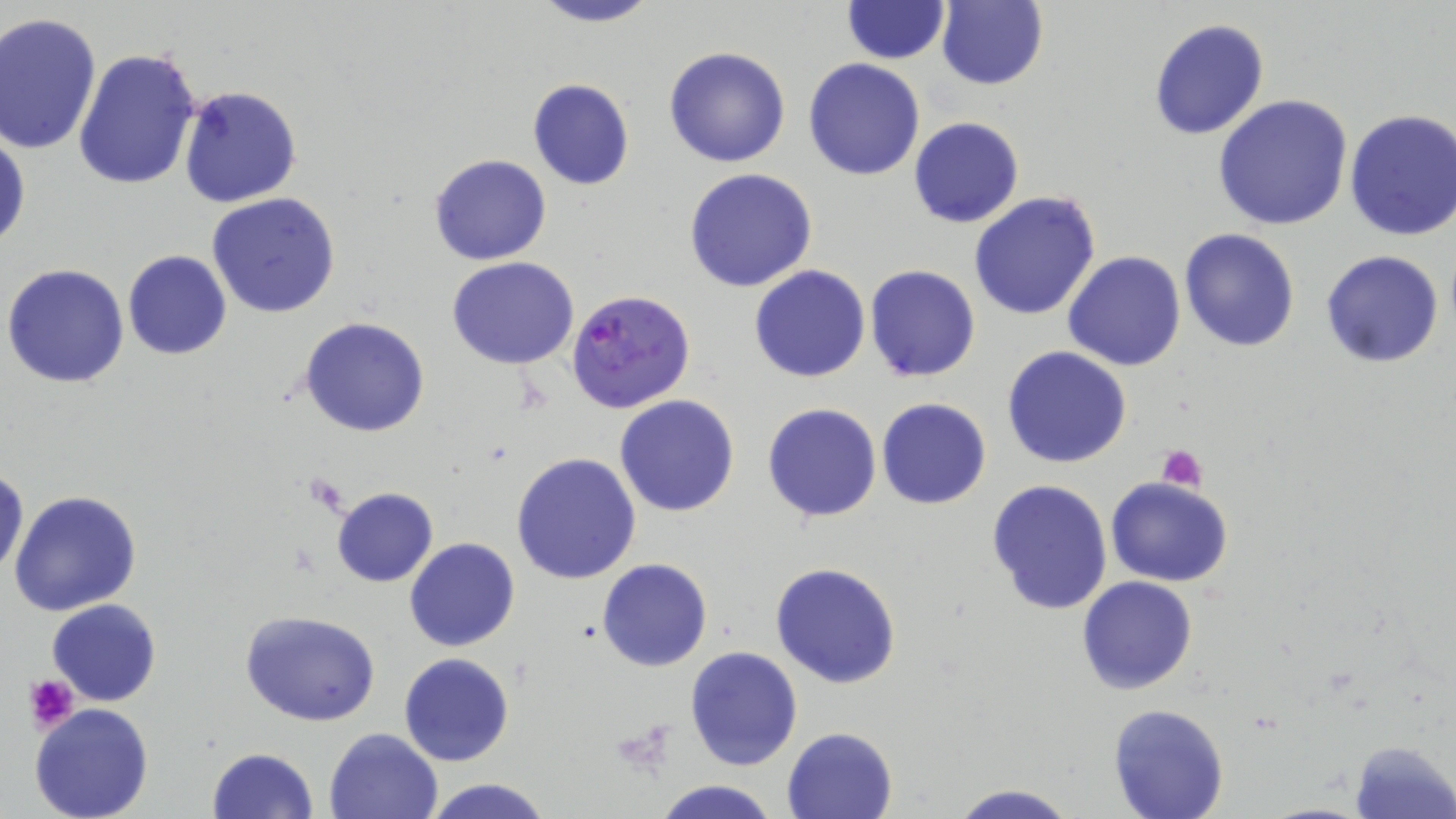

slide-level diagnosis = Plasmodium falciparum
stain = May-Grünwald-Giemsa
preparation = thin blood smear
Plasmodium falciparum-infected red blood cell locations = approximate bounding boxes as [x1, y1, x2, y2] in pixels: [565, 288, 695, 414]
modality = optical microscopy
uninfected red blood cell locations = approximate bounding boxes as [x1, y1, x2, y2] in pixels: [526, 0, 663, 28], [841, 1, 949, 64], [935, 1, 1048, 90], [0, 12, 102, 156], [1149, 17, 1270, 140], [663, 45, 792, 168], [72, 48, 204, 193], [803, 58, 925, 181], [526, 77, 635, 190], [178, 85, 303, 207], [1212, 94, 1353, 231], [1344, 108, 1456, 241], [908, 116, 1024, 230], [0, 125, 30, 254], [935, 140, 1073, 284], [429, 153, 552, 267], [683, 167, 817, 293], [969, 190, 1102, 321], [208, 192, 342, 318], [1179, 227, 1300, 351], [1319, 249, 1446, 368], [122, 250, 232, 359], [1063, 250, 1184, 372], [447, 257, 580, 370], [2, 264, 130, 388], [750, 265, 871, 382], [864, 265, 982, 382], [300, 316, 431, 437], [1002, 346, 1131, 468], [615, 394, 741, 517], [875, 397, 992, 510], [761, 401, 883, 523], [511, 451, 642, 585], [0, 466, 27, 581], [1106, 476, 1235, 586], [986, 479, 1113, 616], [331, 487, 438, 587], [8, 489, 141, 617], [405, 537, 520, 653], [598, 558, 711, 671], [769, 562, 903, 688], [1077, 575, 1198, 695], [48, 598, 162, 707], [240, 610, 381, 726], [684, 646, 802, 770], [398, 653, 516, 767], [30, 702, 156, 819], [1107, 703, 1230, 819], [781, 726, 898, 819], [323, 727, 442, 819], [1349, 739, 1455, 818], [208, 746, 319, 819], [421, 777, 555, 819], [653, 779, 779, 819], [946, 782, 1079, 819]
image size = 1456×819 pixels
magnification = 1000x
platelet locations = approximate bounding boxes as [x1, y1, x2, y2] in pixels: [1156, 444, 1207, 493], [24, 672, 78, 731]
field of view = single